Mark where leukocytes are.
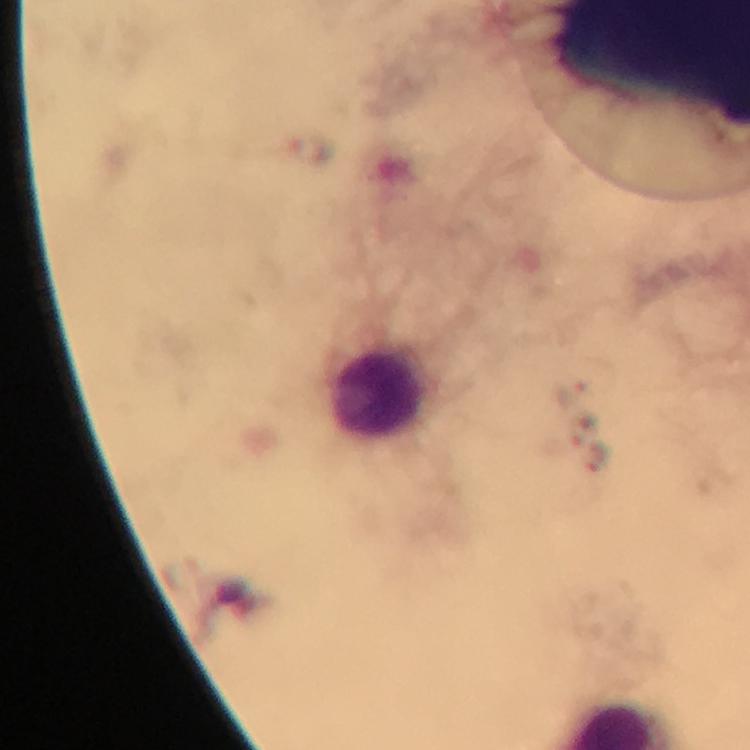

Approximate object centers, in pixels from the top-left corner.
Leukocytes: (x=378, y=391).

Summary:
  - Plasmodium parasites: none detected
  - Cropped from: one field of view
  - Immersion oil: used
  - Magnification: 100x
  - Capture: smartphone camera through the microscope
  - Context: from a malaria diagnostic workup
  - Stain: Giemsa
  - Image size: 750×750 pixels
  - Preparation: thick blood smear